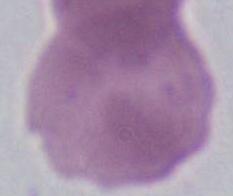
Summary:
  - Magnification: 1000x
  - Identification: erythrocyte
  - Modality: photomicrograph